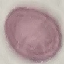

Result: no malaria parasites detected. Cell patch, automatically extracted from a larger field of view and resized to 64 × 64 pixels. Photographed with a smartphone camera at the microscope eyepiece. Thin blood film. Giemsa-stained preparation.